State which parasite is depicted.
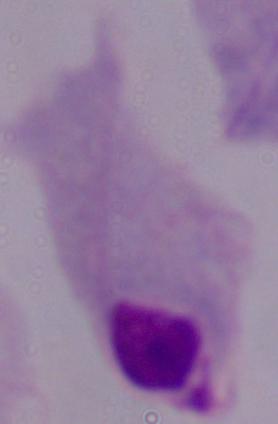

This is a trichomonad.

Summary:
  - Modality: photomicrograph
  - Magnification: 1000x